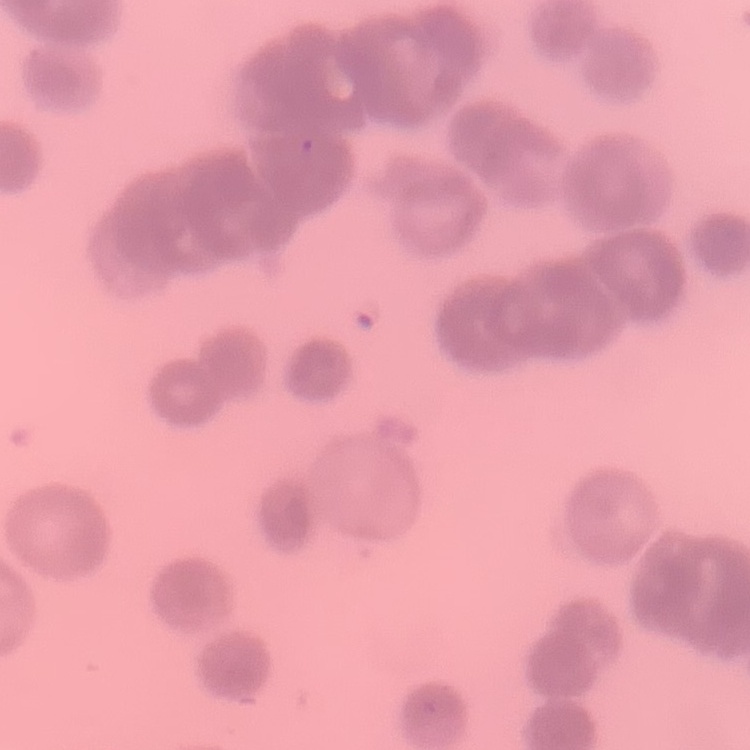
Summary:
  - Red blood cell morphology: rouleaux formation
  - Preparation: thin peripheral smear
  - Image type: one tile cut from a larger photomicrograph
  - Stain: Field's or Giemsa